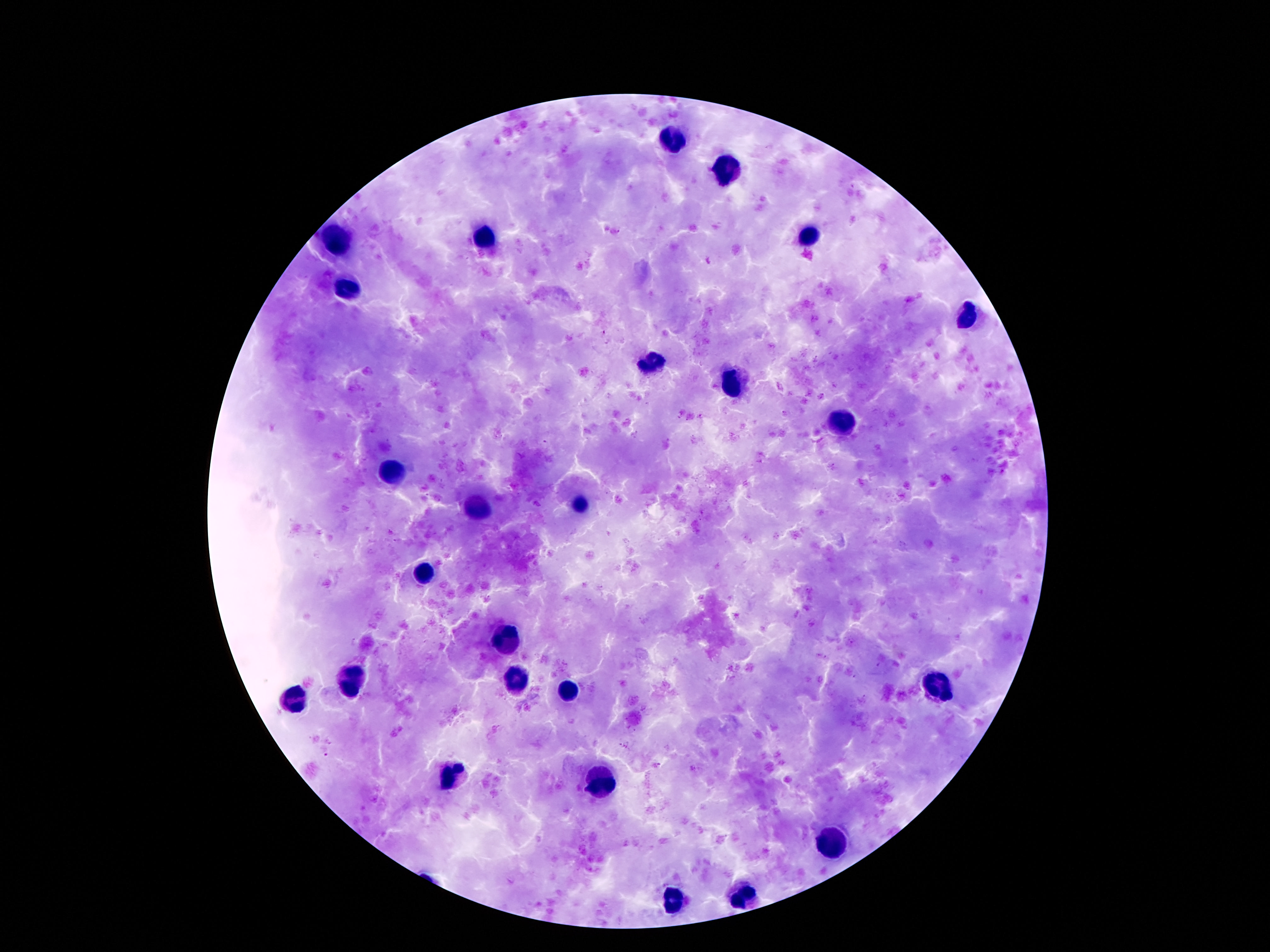
Approximate centers as (x, y) in pixels. Leukocyte locations: (673, 136), (727, 169), (486, 237), (802, 238), (337, 241), (348, 289), (968, 319), (648, 361), (734, 384), (845, 425), (391, 472), (579, 507), (479, 513), (425, 575), (505, 636), (520, 678), (353, 679), (938, 683), (566, 693), (291, 702), (448, 774), (600, 784), (833, 843), (741, 898), (673, 899). Giemsa stain. Patient malaria status: negative. One field from this slide. Photographed through the microscope eyepiece with a smartphone camera. Image is 1270×952 pixels. 100x magnification. Thick peripheral-blood smear.